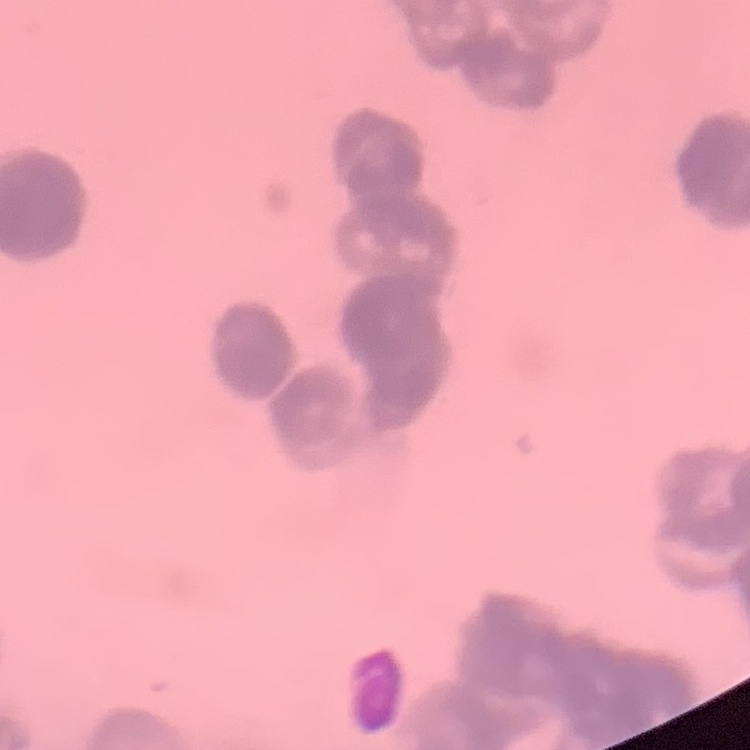

The erythrocytes show rouleaux formation. Thin peripheral smear. Stained with either Field's or Giemsa. Square crop of a larger photomicrograph.